Name the parasite shown.
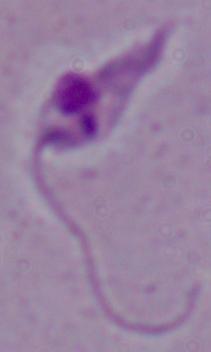
This is Leishmania.

Captured at 1000x magnification. Micrograph.